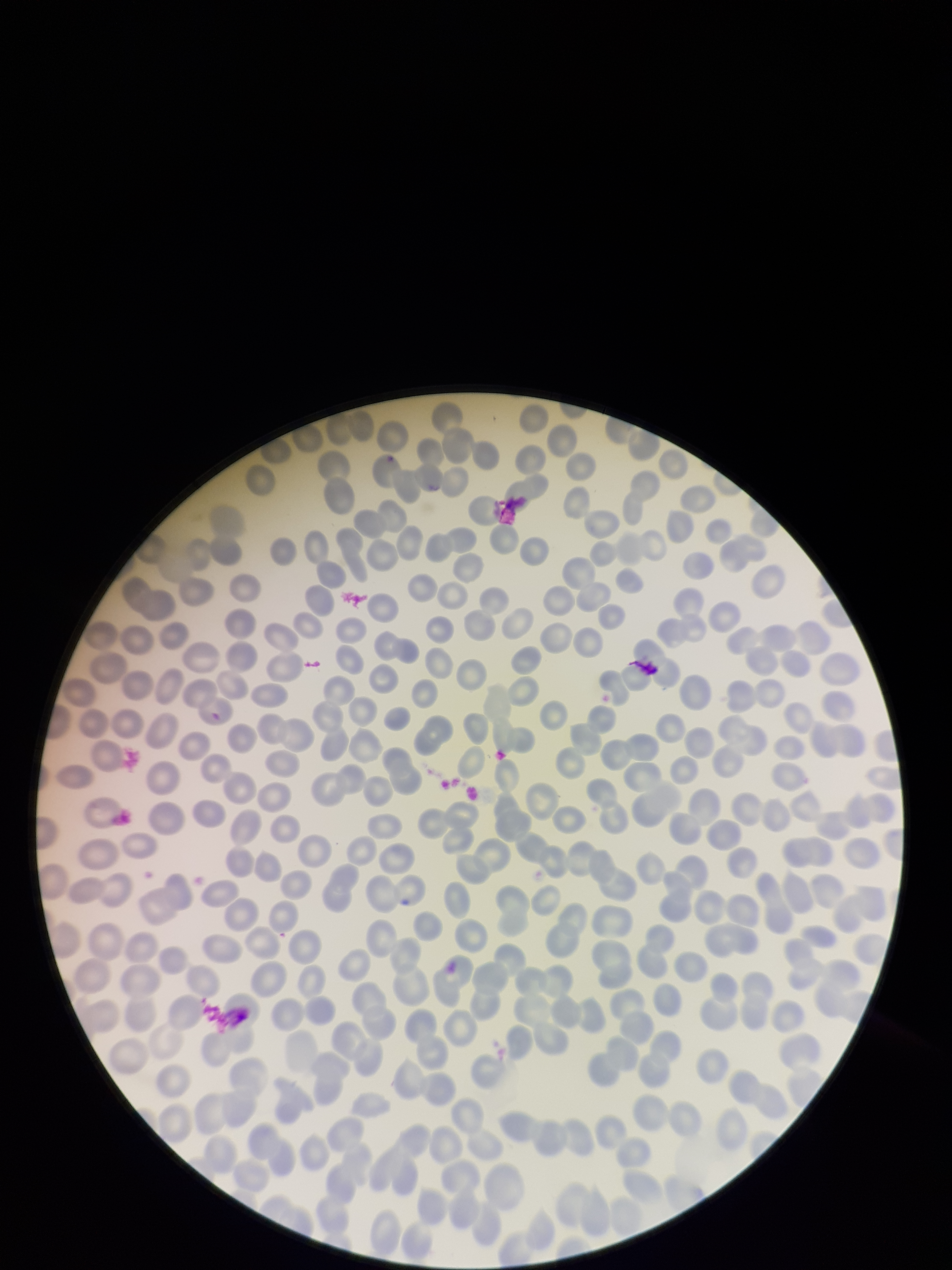
Parasitized red blood cells: none identified. Red blood cell count: 230. Stained with Giemsa. Smartphone photograph taken through the eyepiece of a microscope. Single field of view. Parasitized red blood cell count: 0. Image is 952×1270 pixels. Patient malaria status: negative. Preparation: thin.